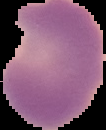

Summary:
  - Image size: 106×130 pixels
  - Image type: cell region segmented out of the field of view; surrounding area masked to black
  - Malaria status: parasitized
  - Preparation: thin blood smear